Assess the morphology of the erythrocytes.
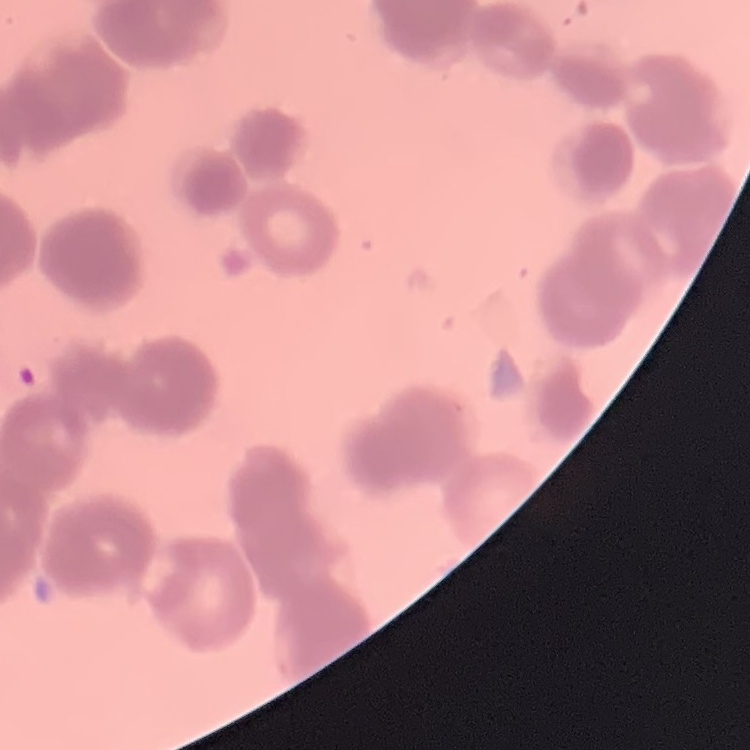
Rouleaux formation.

Thin blood smear. One tile cut from a larger photomicrograph. Field's or Giemsa stain.